Assess for Plasmodium parasites.
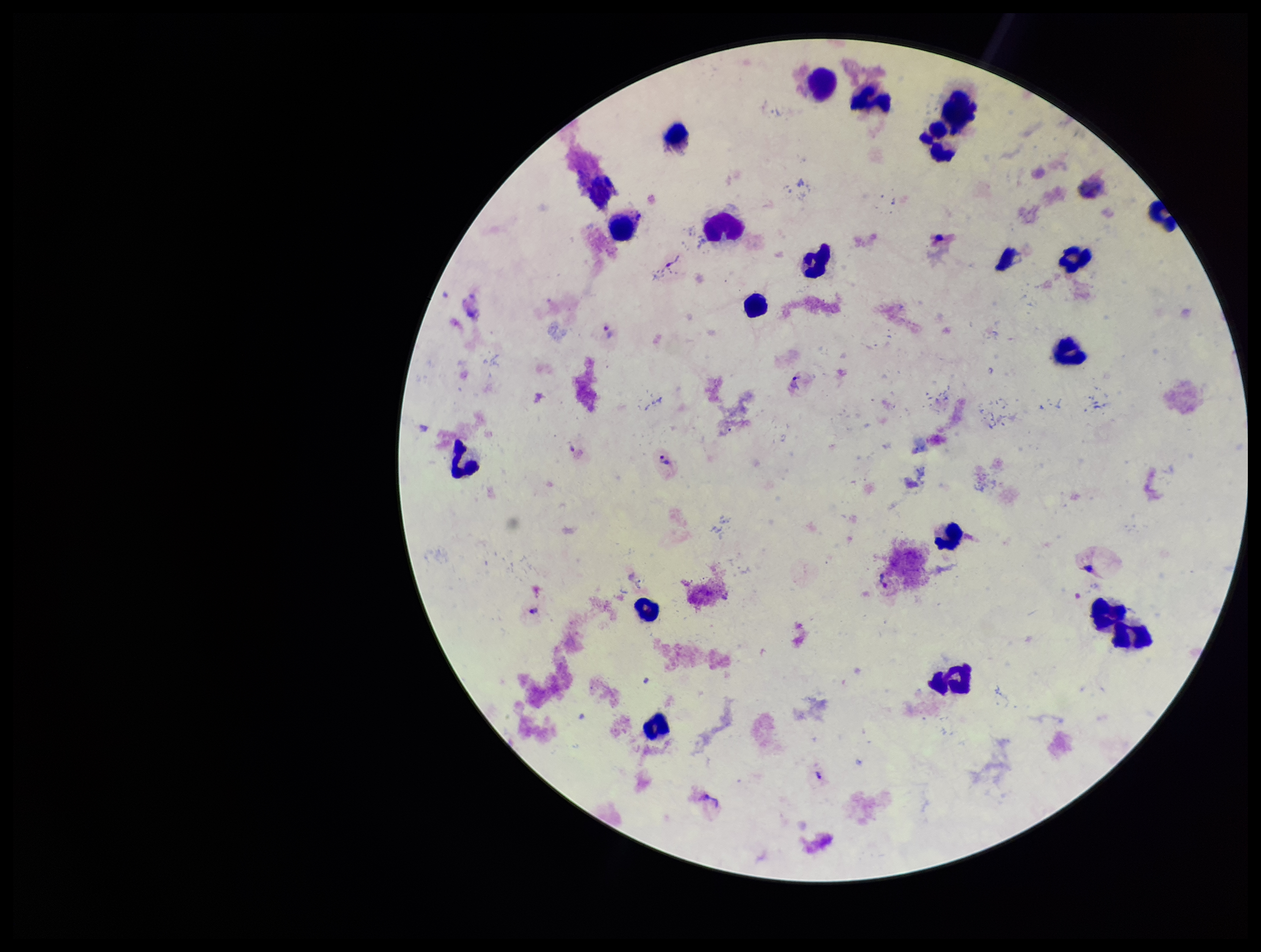
Detected.

Stained with Giemsa. Preparation: thick smear. Single field of view. Species reported for this patient: Plasmodium vivax. Smartphone photograph taken through the eyepiece of a microscope. Image is 1261×952 pixels. Leukocyte count: 21. Patient malaria status: positive. Parasite count: 3.